Assess for malaria.
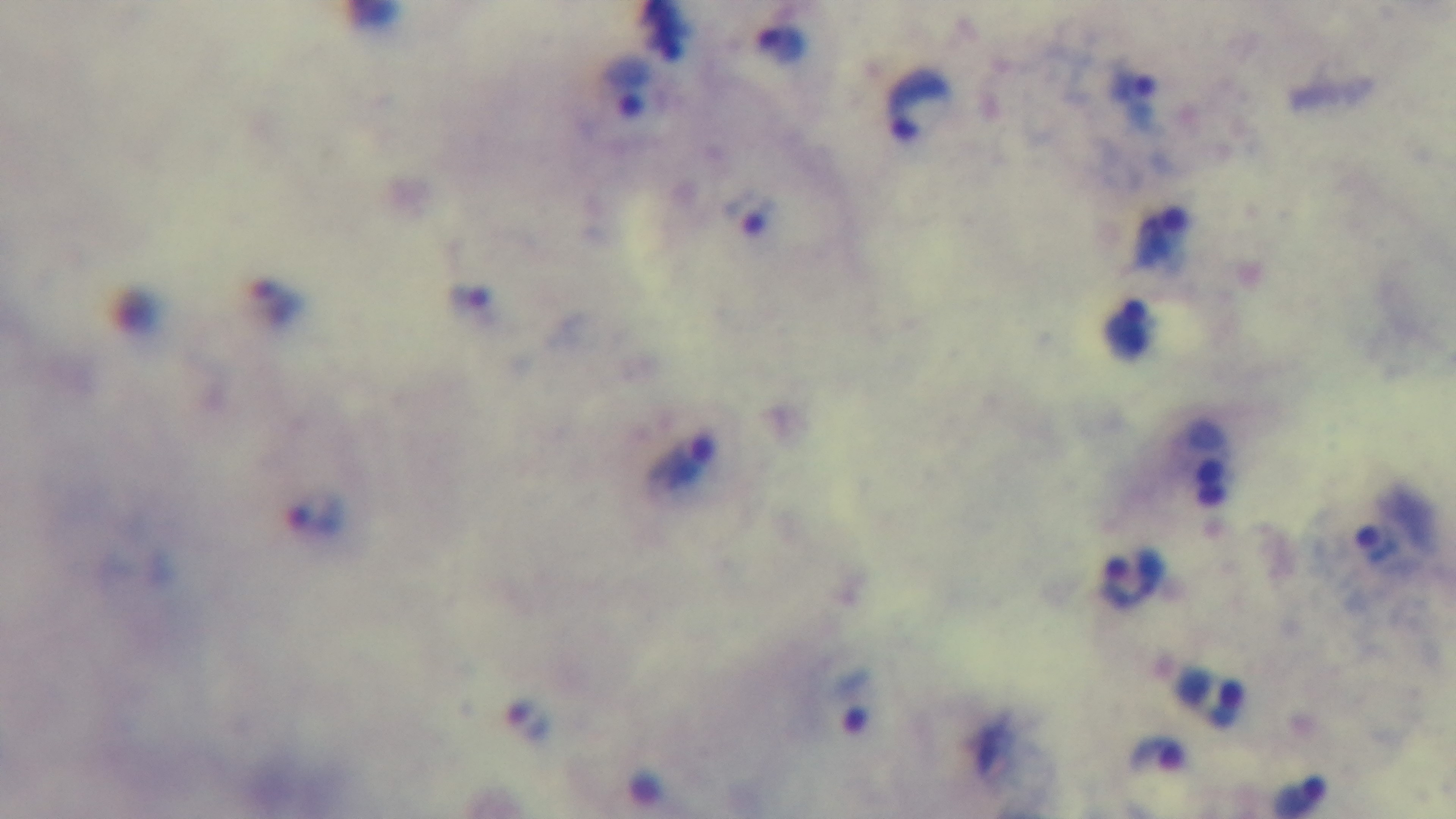
Positive.

capture = mounted 4K digital camera
field of view = single
preparation = thick smear
objective = 100x oil immersion
modality = light microscopy
stain = Giemsa